State which parasite is depicted.
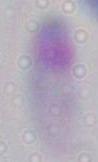

This is Toxoplasma gondii.

Photomicrograph. 1000x magnification.